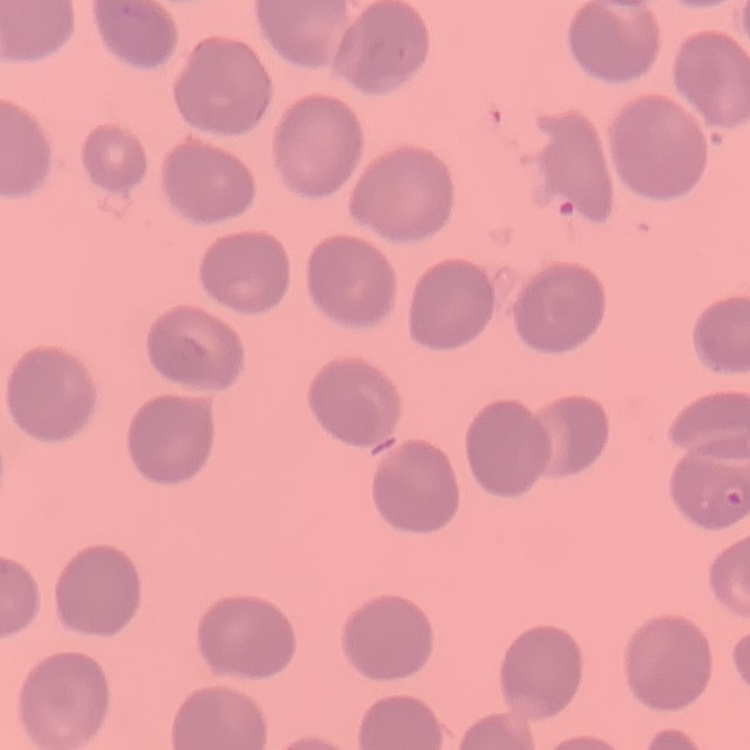

Summary:
  - Erythrocyte morphology: no rouleaux formation
  - Image type: square crop of a larger photomicrograph
  - Stain: Field's or Giemsa
  - Preparation: thin blood film